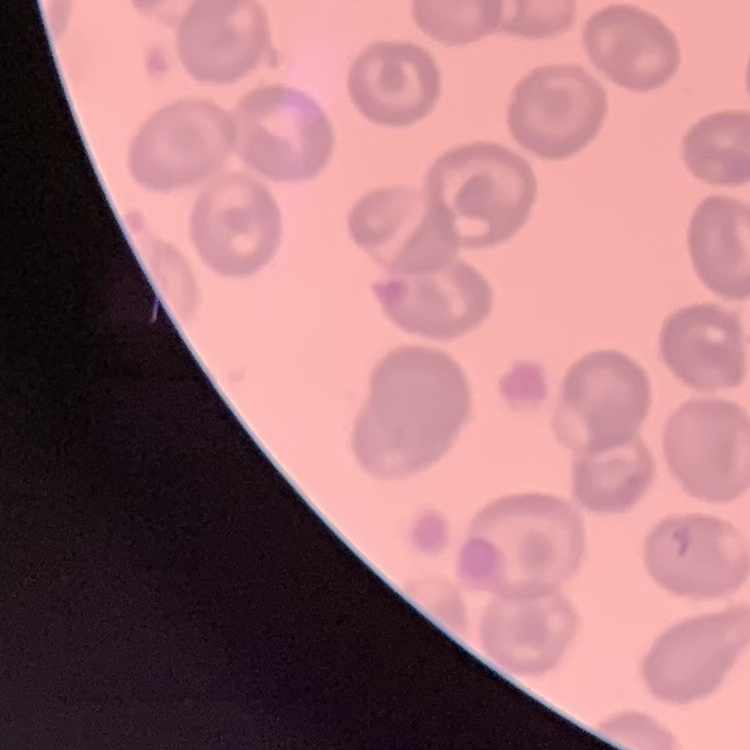

The erythrocytes exhibit no rouleaux formation. Square crop of a larger photomicrograph. Stained with either Field's or Giemsa. Thin peripheral smear.